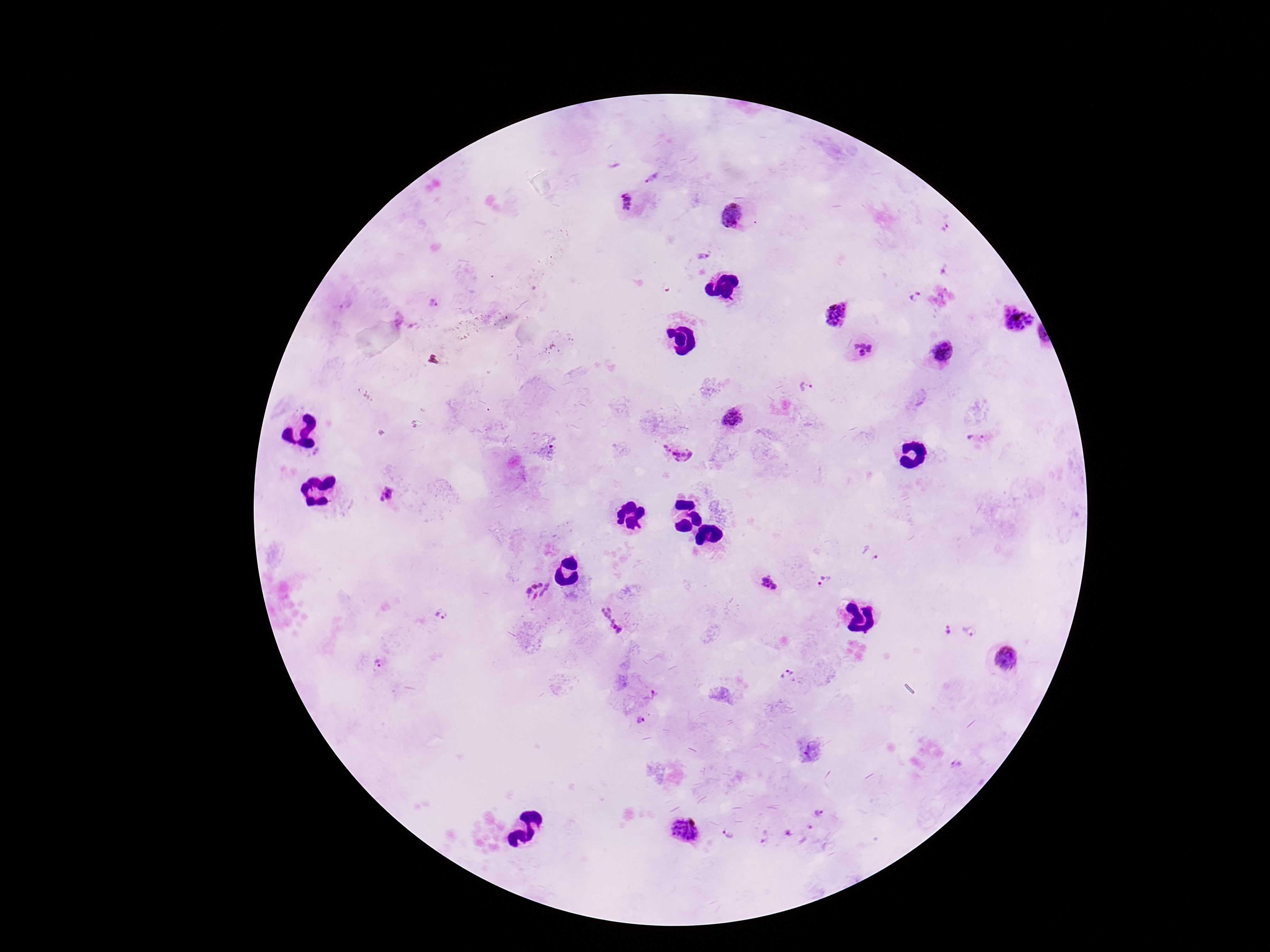

Approximate centers as {x, y} in pixels. Plasmodium parasite locations: {649, 178}, {626, 202}, {733, 214}, {945, 229}, {702, 257}, {946, 271}, {915, 296}, {345, 305}, {433, 305}, {836, 315}, {399, 318}, {1017, 320}, {863, 349}, {942, 351}, {806, 386}, {733, 417}, {976, 438}, {665, 448}, {549, 450}, {318, 452}, {682, 456}, {386, 494}, {870, 555}, {824, 582}, {769, 585}, {538, 591}, {441, 615}, {611, 620}, {947, 630}, {970, 632}, {1007, 658}, {378, 663}, {787, 674}, {651, 696}, {640, 720}, {958, 765}, {820, 812}, {809, 827}, {685, 829}, {729, 834}, {789, 834}, {764, 836}. 100x magnification. Giemsa-stained preparation. Smartphone photograph taken through the microscope eyepiece. Image is 1270×952 pixels. Thick blood film. Single field of view. Patient malaria status: infected.